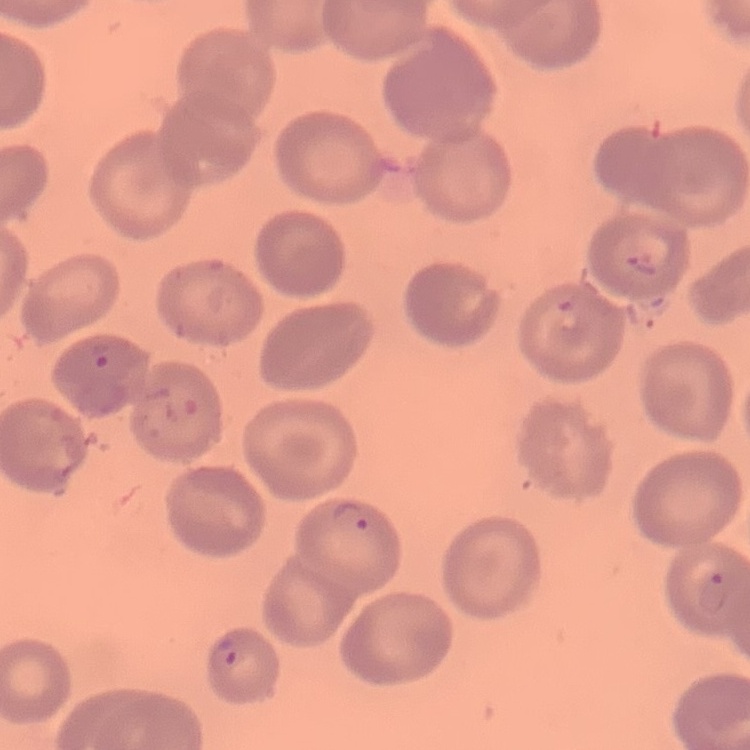
erythrocyte morphology = no rouleaux formation
image type = one tile cut from a larger photomicrograph
stain = Field's or Giemsa
preparation = thin blood smear